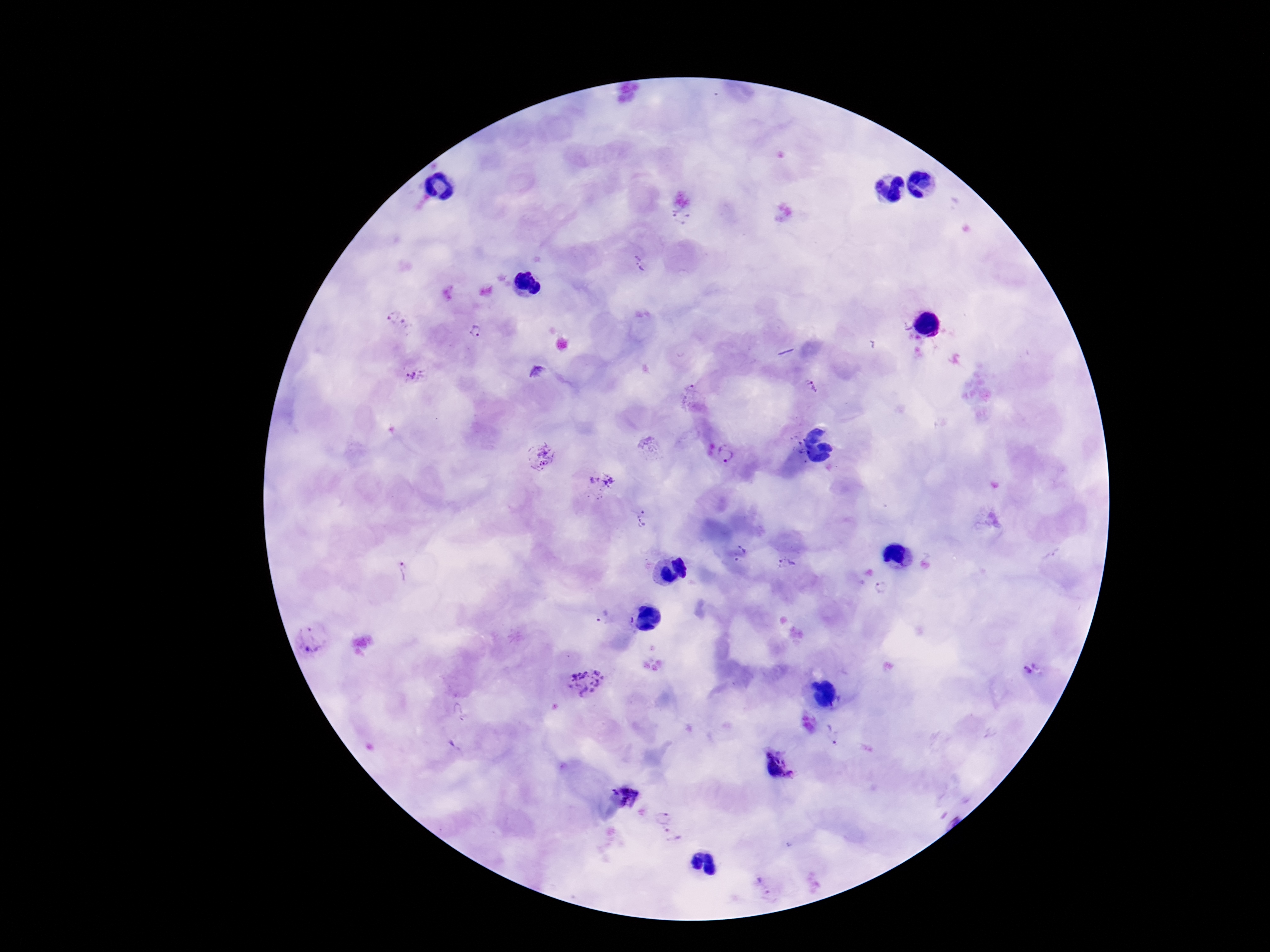
Approximate centers as [x, y] in pixels. Plasmodium parasite locations: [681, 218], [641, 263], [397, 320], [473, 334], [537, 374], [415, 375], [812, 386], [692, 390], [726, 454], [540, 456], [600, 479], [642, 518], [742, 554], [787, 564], [407, 569], [881, 588], [603, 618], [313, 640], [1030, 668], [586, 681], [832, 735], [776, 764], [663, 815], [673, 836], [763, 886]. Thick peripheral-blood smear. Single field of view. Patient malaria status: positive. Giemsa stain. 100x magnification. Image is 1270×952 pixels. Smartphone photograph taken through the microscope eyepiece.